Give the extent of all Plasmodium falciparum-infected red blood cells.
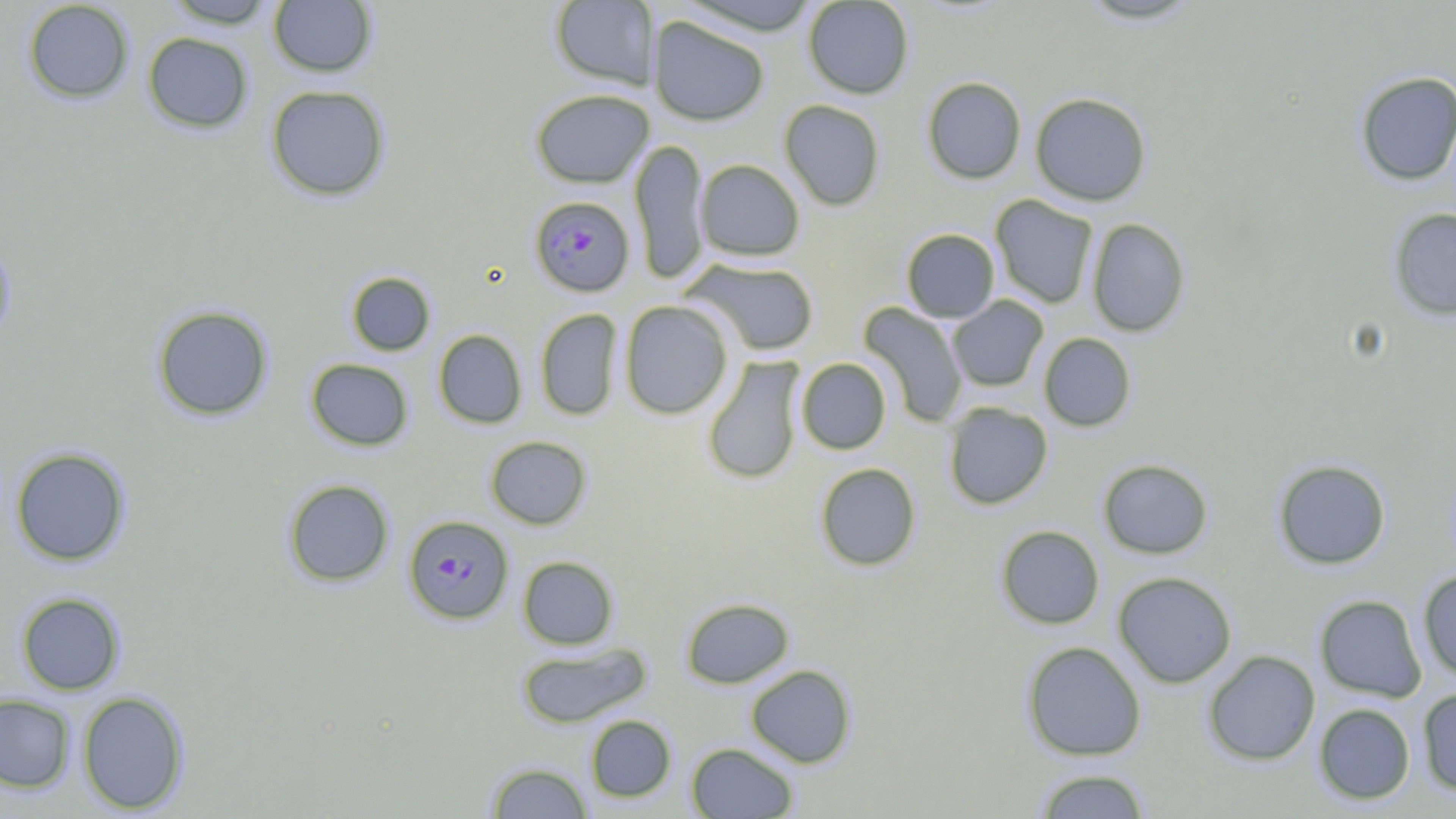
Approximate bounding boxes as (x1, y1, x2, y2) in pixels.
Plasmodium falciparum-infected red blood cells: (529, 195, 635, 296), (403, 514, 514, 625).

Uninfected red blood cell locations: (161, 0, 279, 28), (676, 0, 823, 35), (802, 0, 915, 99), (1073, 0, 1207, 26), (22, 1, 134, 104), (268, 1, 378, 77), (550, 1, 660, 90), (648, 16, 770, 125), (142, 32, 254, 133), (1354, 71, 1456, 186), (922, 76, 1026, 184), (265, 84, 391, 201), (529, 88, 653, 187), (1030, 92, 1152, 206), (779, 100, 885, 211), (629, 138, 710, 284), (695, 159, 805, 261), (990, 195, 1098, 309), (1388, 207, 1456, 320), (1086, 218, 1190, 337), (900, 228, 1000, 322), (0, 233, 17, 349), (681, 257, 820, 356), (345, 271, 436, 356), (947, 296, 1049, 392), (619, 300, 734, 419), (858, 302, 969, 428), (151, 305, 274, 421), (534, 308, 622, 420), (433, 329, 527, 429), (1038, 333, 1137, 432), (701, 357, 805, 485), (305, 358, 414, 451), (796, 358, 891, 454), (943, 402, 1053, 509), (484, 436, 592, 529), (9, 447, 131, 566), (1098, 458, 1213, 559), (1272, 459, 1391, 569), (815, 462, 922, 571), (282, 479, 395, 587), (995, 525, 1105, 629), (517, 556, 619, 650), (1417, 570, 1456, 681), (1112, 571, 1237, 687), (15, 591, 126, 695), (1314, 594, 1427, 702), (680, 597, 794, 688), (1021, 641, 1146, 761), (517, 642, 651, 728), (1202, 650, 1320, 765), (745, 664, 857, 768), (1417, 687, 1456, 796), (76, 691, 190, 814), (0, 693, 76, 792), (1313, 703, 1416, 805), (585, 715, 676, 802), (686, 741, 799, 818), (485, 761, 594, 818), (1032, 769, 1151, 818). Slide-level diagnosis: Plasmodium falciparum. Single field of view. Image is 1456×819 pixels. 1000x magnification. Light microscopy. May-Grünwald-Giemsa-stained preparation. Thin blood smear.